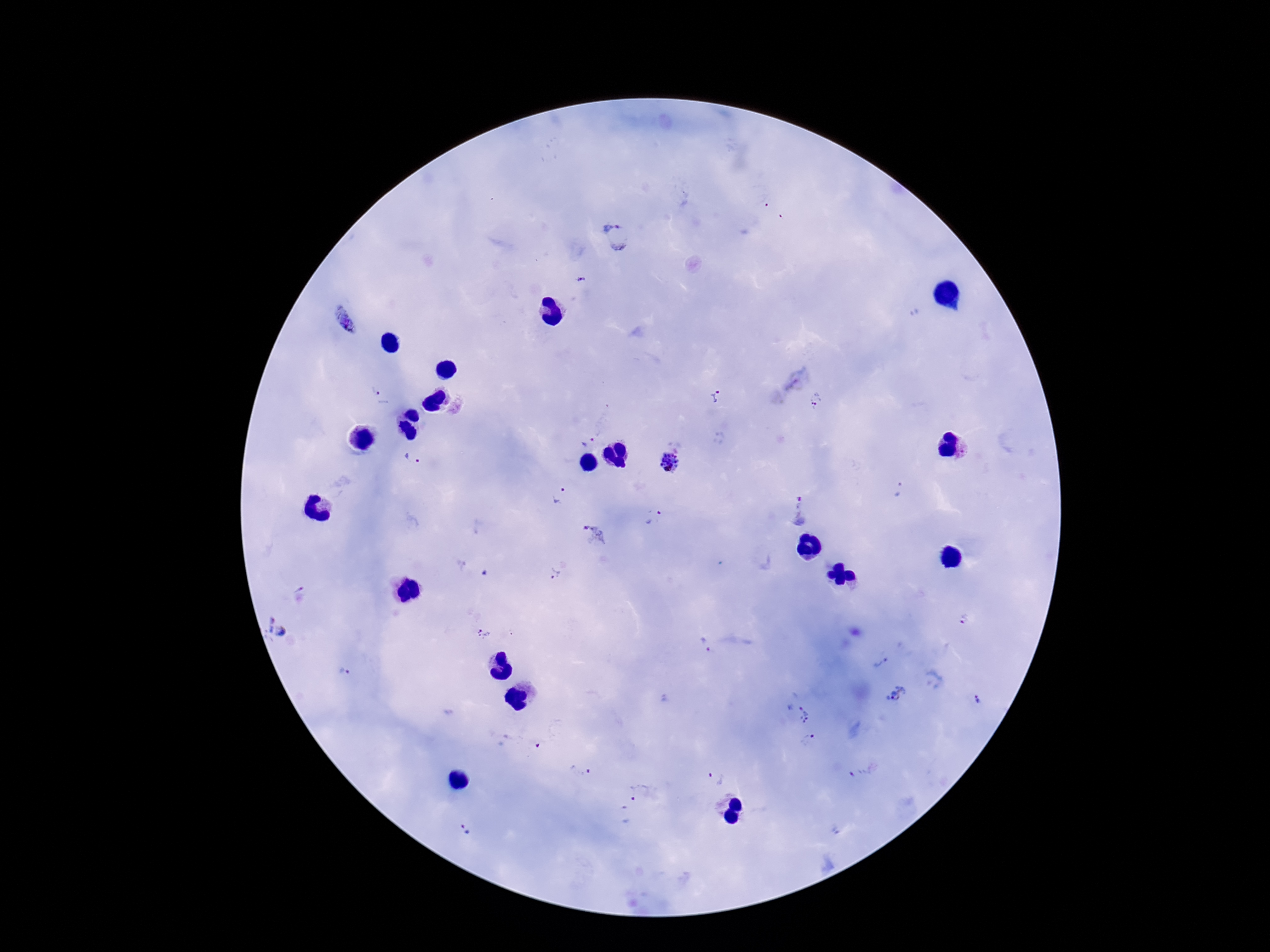

Approximate centers as [x, y] in pixels.
Summary:
  - Plasmodium parasite locations: [617, 236], [582, 280], [344, 320], [375, 391], [716, 396], [815, 400], [586, 441], [412, 458], [669, 462], [901, 489], [560, 496], [799, 512], [653, 518], [595, 536], [553, 575], [964, 618], [278, 627], [483, 635], [706, 645], [880, 663], [345, 672], [898, 694], [976, 700], [797, 715], [810, 740], [581, 769], [861, 771], [715, 778], [638, 792], [624, 815], [464, 829]
  - Magnification: 100x
  - Stain: Giemsa
  - Patient malaria status: positive
  - Field of view: one from this slide
  - Capture: smartphone camera through the microscope eyepiece
  - Image size: 1270×952 pixels
  - Preparation: thick blood film